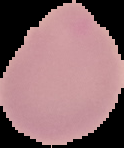
From a thin blood film. Malaria status: uninfected. Cell region segmented out of the field of view; the surrounding area is masked to black. Image is 124×148 pixels.